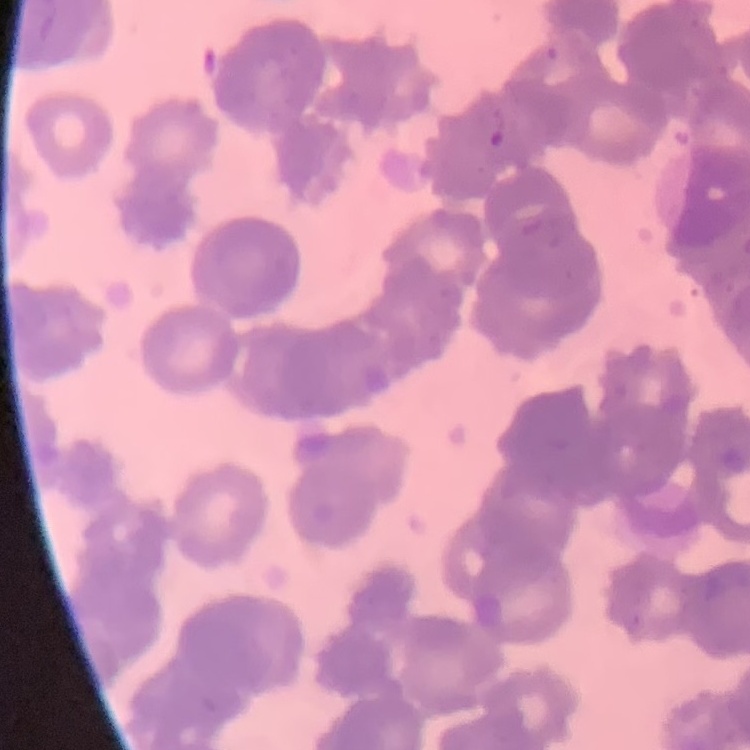

red blood cell morphology = rouleaux formation
image type = square crop of a larger photomicrograph
preparation = thin blood smear
stain = Field's or Giemsa